Locate every Plasmodium parasite.
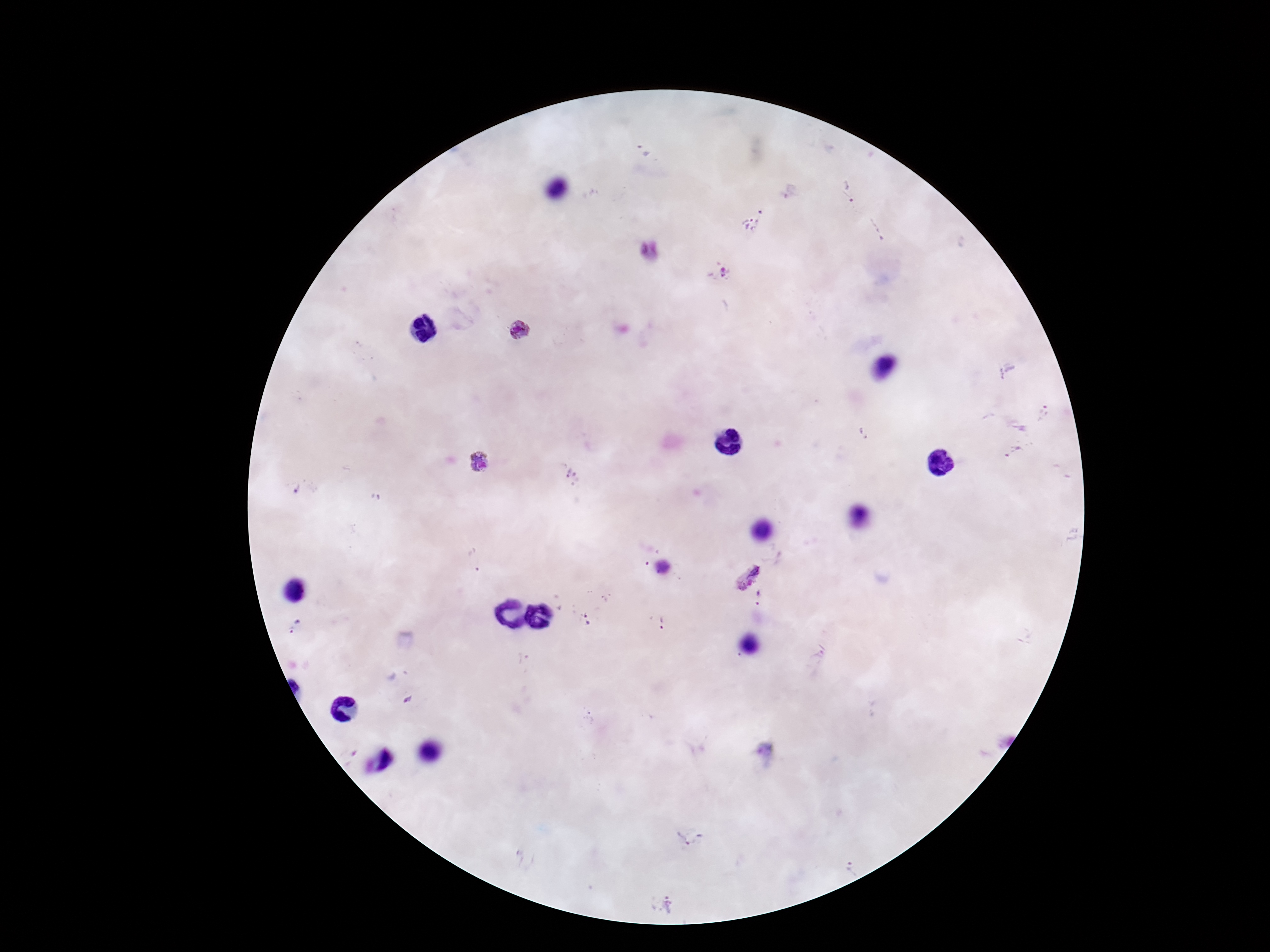

Approximate centers as (x, y) in pixels.
Plasmodium parasites: (642, 150), (847, 192), (753, 220), (876, 229), (651, 253), (717, 272), (520, 331), (1044, 414), (864, 434), (1015, 454), (478, 462), (573, 475), (745, 572), (759, 598), (585, 619), (662, 622), (295, 628), (408, 700), (690, 840), (852, 870), (661, 904).

Summary:
  - Preparation: thick peripheral-blood smear
  - Capture: smartphone camera through the microscope eyepiece
  - Stain: Giemsa
  - Image size: 1270×952 pixels
  - Field of view: one from this slide
  - Magnification: 100x
  - Patient malaria status: infected